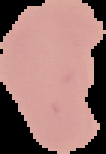
Summary:
  - Image size: 106×154 pixels
  - Image type: segmented cell region on a black background
  - Preparation: thin blood smear
  - Malaria status: uninfected